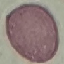

result = no malaria parasites detected
stain = Giemsa
capture = smartphone camera at the microscope eyepiece
image type = automatically extracted cell patch, resized to 64 × 64 pixels
preparation = thin blood film